Classify this cell by malaria status.
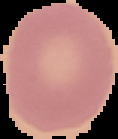
Uninfected.

Cell region segmented out of the field of view; the surrounding area is masked to black. From a thin blood smear. Image is 118×139 pixels.